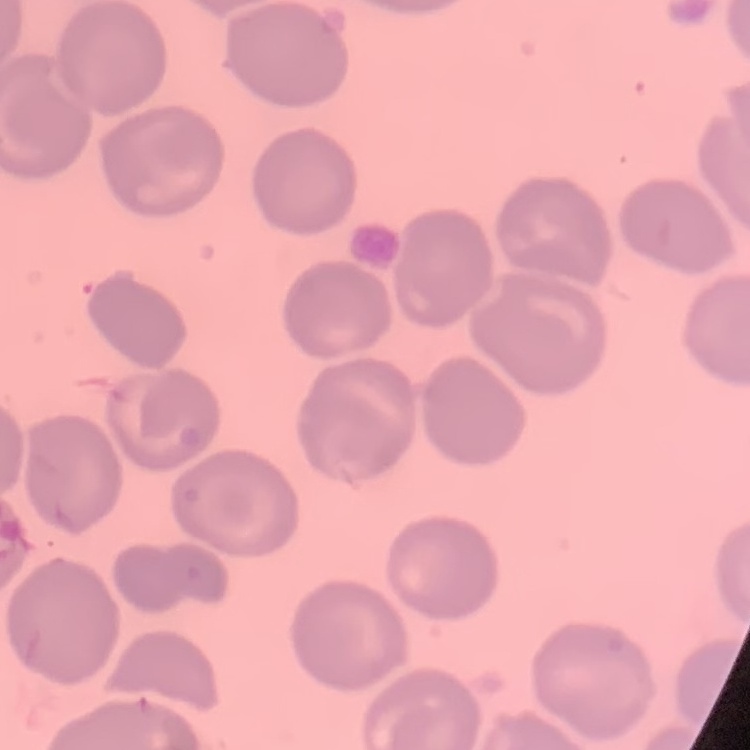
Summary:
  - Red blood cell morphology: no rouleaux formation
  - Stain: Field's or Giemsa
  - Preparation: thin blood film
  - Image type: one tile cut from a larger photomicrograph